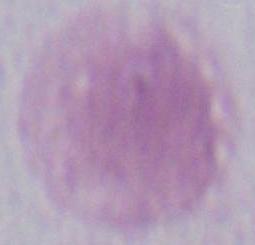

Photomicrograph. 1000x magnification. A red blood cell is seen.